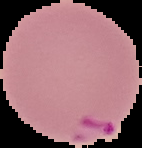

preparation: thin blood smear
malaria_status: parasitized
image_type: segmented cell region with the area outside set to black
image_size: 142×148 pixels